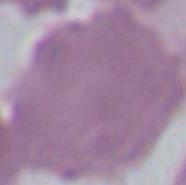

modality = photomicrograph
identification = red blood cell
magnification = 1000x